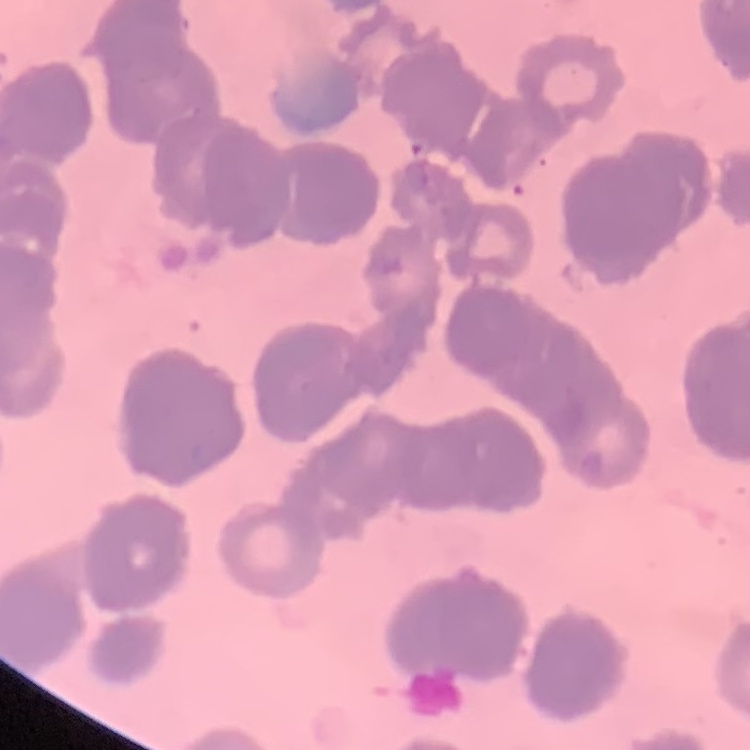

Summary:
  - Red blood cell morphology: rouleaux formation
  - Preparation: thin blood film
  - Stain: Field's or Giemsa
  - Image type: square crop of a larger photomicrograph